Identify the parasite.
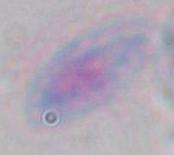
This is Toxoplasma gondii.

Summary:
  - Modality: photomicrograph
  - Magnification: 1000x